Report the malaria status of this cell.
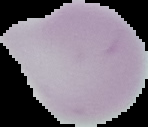
It is uninfected.

Summary:
  - Image size: 148×127 pixels
  - Image type: segmented cell region with the area outside set to black
  - Preparation: thin blood film